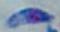

Summary:
  - Magnification: 1000x
  - Modality: micrograph
  - Identification: Toxoplasma gondii